Outline each blood parasite and name the species.
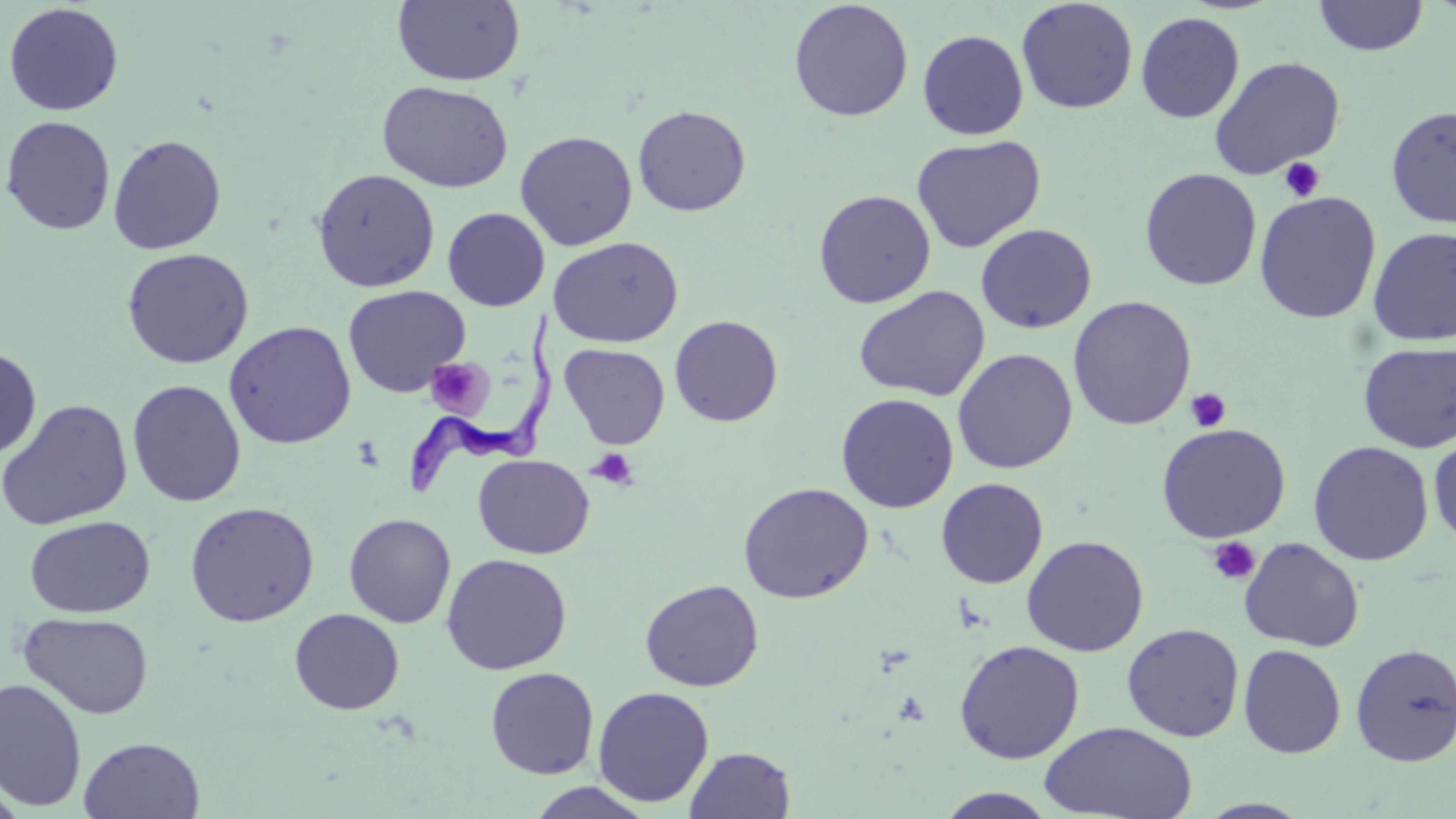
Approximate bounding boxes as (x1,y1)-(x2,y2) corner pairs in pixels.
Trypanosoma brucei: (387,307)-(563,498).
No Plasmodium falciparum, Plasmodium ovale, Plasmodium malariae, Plasmodium vivax, or Babesia divergens observed.

Uninfected red blood cell locations: (1313,0)-(1429,56), (392,1)-(525,87), (788,1)-(914,122), (1016,1)-(1138,114), (2,3)-(124,117), (1135,11)-(1245,124), (917,30)-(1029,140), (1210,55)-(1346,178), (377,80)-(514,192), (632,104)-(751,216), (1385,105)-(1456,229), (1,115)-(117,237), (515,130)-(638,251), (107,134)-(227,255), (911,134)-(1046,253), (311,168)-(440,293), (1139,168)-(1262,291), (813,189)-(936,308), (1254,192)-(1381,324), (442,207)-(550,311), (975,223)-(1097,334), (1366,226)-(1456,346), (548,236)-(684,348), (121,247)-(254,369), (342,285)-(470,398), (853,285)-(990,402), (1067,295)-(1197,431), (669,314)-(783,427), (223,320)-(357,450), (1357,341)-(1456,453), (559,343)-(670,450), (0,346)-(41,459), (952,348)-(1078,474), (127,379)-(246,507), (836,393)-(959,513), (0,398)-(133,530), (1156,423)-(1291,543), (1428,432)-(1456,546), (1308,440)-(1434,566), (472,454)-(595,559), (936,478)-(1049,588), (737,481)-(874,604), (184,501)-(320,627), (343,513)-(456,628), (24,515)-(155,618), (1021,534)-(1149,657), (1239,537)-(1364,652), (441,553)-(572,675), (640,578)-(764,691), (289,608)-(405,715), (18,612)-(155,720), (1121,623)-(1245,742), (954,639)-(1085,764), (1350,642)-(1456,767), (1238,644)-(1347,758), (485,667)-(599,779), (0,676)-(87,811), (593,686)-(714,807), (1039,721)-(1198,819), (78,736)-(206,819), (685,746)-(796,818), (522,781)-(657,818), (934,788)-(1061,818). Platelet locations: (1279,157)-(1325,202), (425,358)-(492,418), (1185,387)-(1231,432), (586,447)-(638,489), (1206,536)-(1261,586). Slide-level diagnosis: Trypanosoma brucei. 1000x magnification. Light microscopy. May-Grünwald-Giemsa-stained preparation. Thin blood film. Image is 1456×819 pixels. One field of a larger specimen.